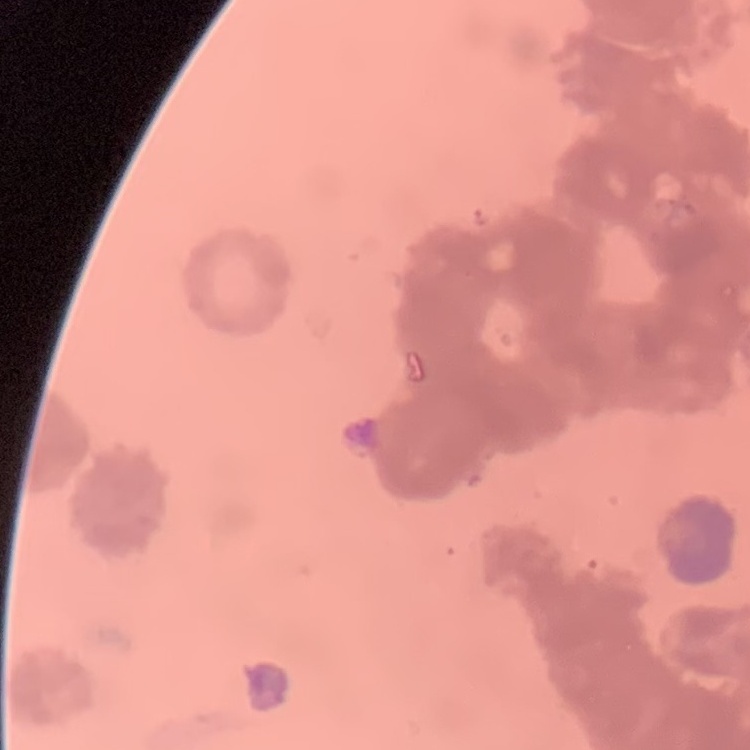 The erythrocytes exhibit rouleaux formation. Field's or Giemsa stain. Thin blood smear. One tile cut from a larger photomicrograph.